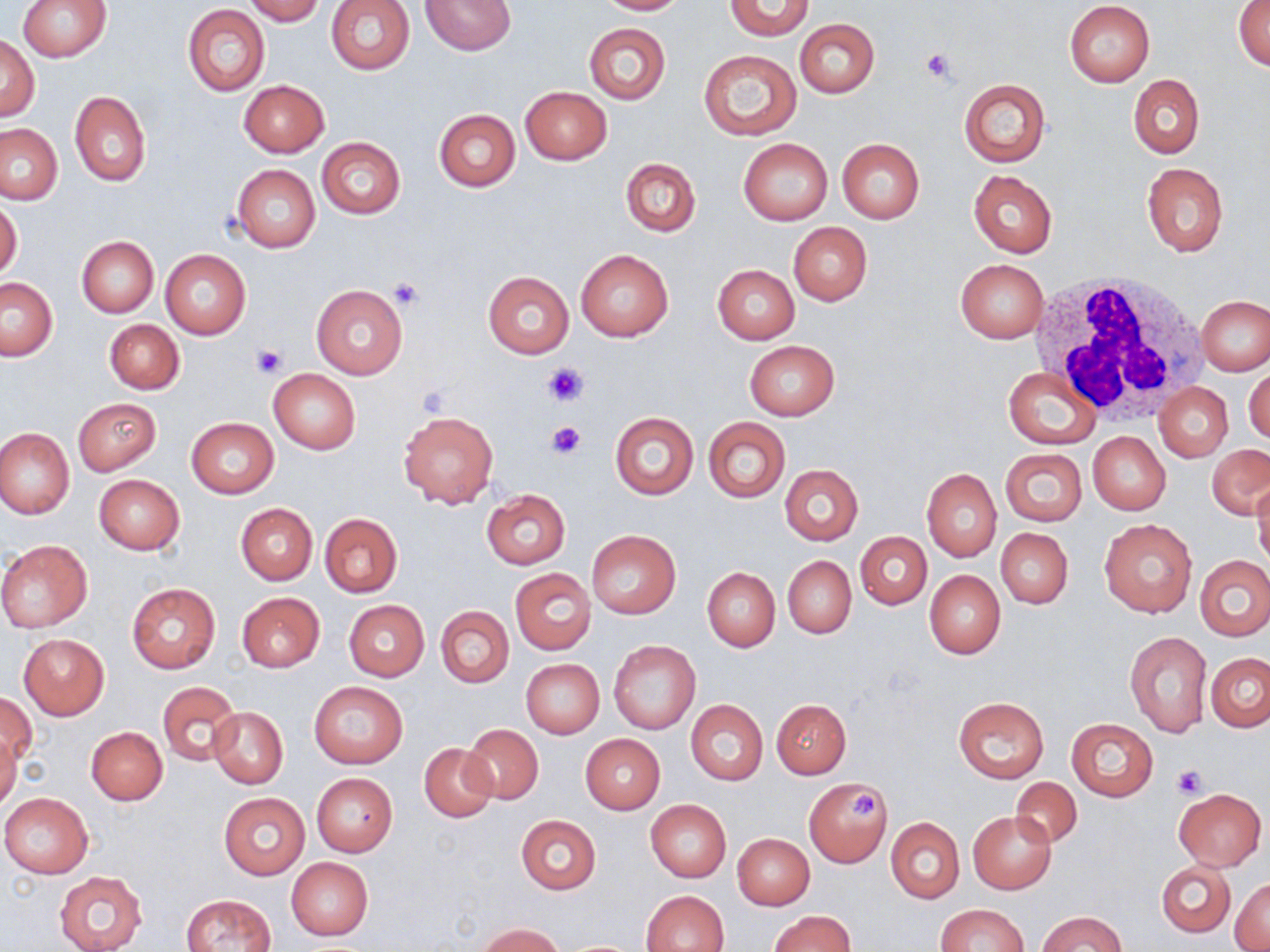 Approximate bounding boxes as (x1,y1)-(x2,y2) corner pairs in pixels. White blood cell locations: (1027,270)-(1211,423). Platelet locations: (920,47)-(959,86), (388,279)-(425,312), (250,343)-(287,378), (546,364)-(589,406), (548,421)-(586,458), (1171,764)-(1207,798), (851,791)-(878,821). Uninfected red blood cell locations: (17,0)-(111,61), (245,0)-(323,24), (421,0)-(516,54), (595,0)-(686,15), (725,0)-(813,40), (326,1)-(414,75), (1234,1)-(1270,73), (1065,2)-(1154,86), (182,5)-(269,97), (795,18)-(879,98), (583,22)-(670,105), (0,37)-(39,120), (698,50)-(802,139), (1129,75)-(1205,159), (959,78)-(1051,167), (238,80)-(329,157), (520,86)-(612,164), (69,91)-(151,185), (433,109)-(520,192), (0,123)-(64,205), (317,138)-(406,218), (738,138)-(834,225), (836,138)-(925,224), (621,157)-(701,236), (1141,163)-(1228,257), (232,165)-(319,252), (967,170)-(1058,257), (0,200)-(23,280), (788,222)-(872,306), (75,236)-(158,318), (575,248)-(674,342), (160,249)-(252,340), (955,259)-(1049,343), (713,265)-(800,345), (483,272)-(574,358), (1,278)-(58,360), (311,284)-(407,380), (1197,296)-(1270,376), (104,319)-(184,394), (744,340)-(838,420), (1245,364)-(1270,446), (1004,367)-(1100,448), (270,370)-(359,452), (1155,383)-(1233,462), (73,398)-(162,475), (399,411)-(498,509), (610,412)-(698,499), (703,417)-(790,503), (186,418)-(279,498), (0,427)-(75,519), (1088,432)-(1171,515), (1207,443)-(1270,520), (1001,448)-(1087,526), (779,463)-(864,546), (922,467)-(1001,561), (93,474)-(185,554), (1251,477)-(1270,569), (481,490)-(570,569), (236,503)-(317,584), (320,513)-(403,597), (1100,520)-(1197,617), (996,527)-(1074,609), (586,530)-(680,619), (856,531)-(931,609), (0,540)-(93,632), (1195,554)-(1269,640), (783,556)-(856,638), (701,566)-(780,651), (510,568)-(595,655), (924,569)-(1006,659), (125,583)-(221,675), (236,593)-(325,672), (343,600)-(429,681), (437,606)-(513,688), (1124,632)-(1213,737), (18,634)-(109,720), (608,639)-(700,734), (1206,653)-(1270,732), (521,659)-(604,737), (308,680)-(408,768), (157,681)-(240,766), (1,692)-(36,767), (954,696)-(1049,784), (771,698)-(851,778), (686,700)-(767,785), (208,707)-(288,789), (1068,719)-(1157,801), (463,724)-(544,805), (86,726)-(168,805), (0,731)-(20,811), (581,734)-(665,814), (420,742)-(498,822), (311,772)-(398,856), (804,777)-(893,867), (1009,777)-(1082,848), (1174,787)-(1265,871), (0,792)-(93,878), (218,792)-(310,879), (645,799)-(731,883), (969,812)-(1055,892), (516,815)-(601,894), (886,817)-(964,903), (733,833)-(814,910), (286,857)-(373,941), (1158,861)-(1234,936), (54,870)-(148,952), (1231,880)-(1270,950), (642,890)-(729,952), (180,893)-(277,951), (935,903)-(1027,952), (769,909)-(855,951), (1039,911)-(1124,951), (477,924)-(566,952). Slide-level diagnosis: negative for blood parasites. Image is 1270×952 pixels. 1000x magnification. Thin blood film. May-Grünwald-Giemsa stain. Single field of view. Optical microscopy.